Describe the morphology of the red blood cells.
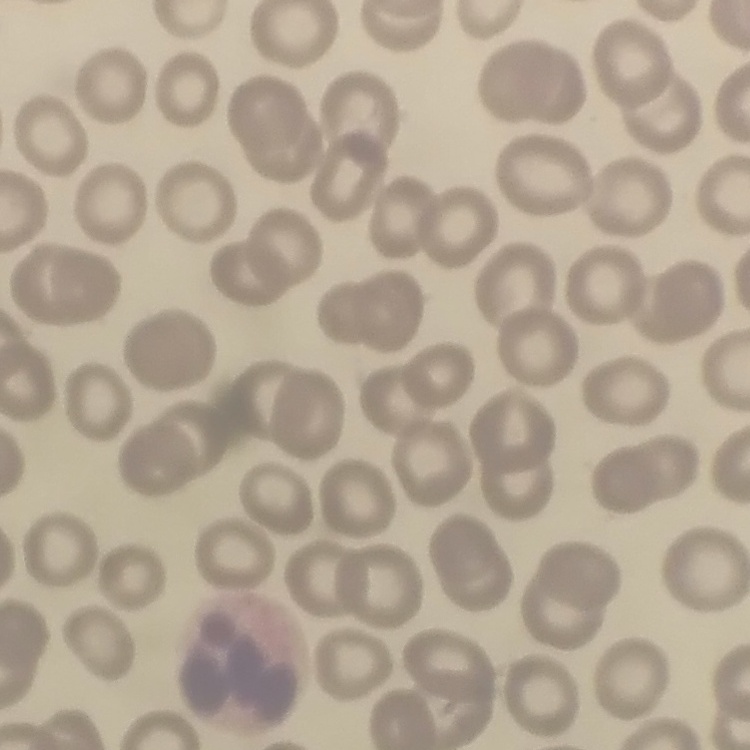
They show no rouleaux formation.

Summary:
  - Preparation: thin blood film
  - Stain: Field's or Giemsa
  - Image type: square crop of a larger photomicrograph